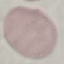 Malaria status: uninfected. Automatically extracted cell patch, resized to 64 × 64 pixels. Giemsa-stained preparation. Acquired by smartphone through the microscope eyepiece. Thin blood film.